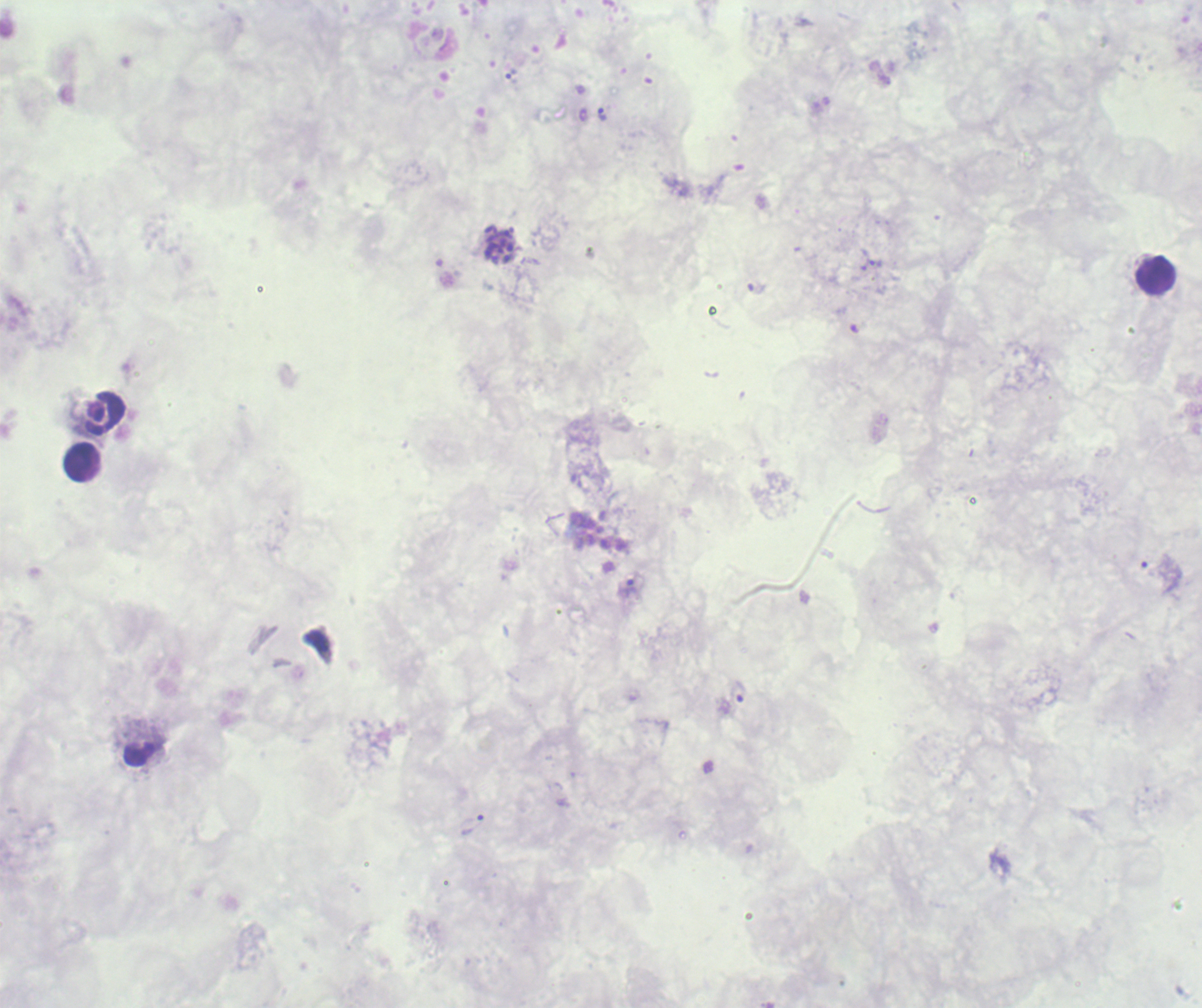
Approximate centers as {x, y} in pixels.
Summary:
  - Schizont locations: {499, 245}
  - Trophozoite locations: {602, 115}, {876, 263}, {629, 588}, {737, 692}, {473, 825}
  - Leukocyte locations: {1156, 275}, {106, 414}, {80, 461}, {139, 753}
  - Life-cycle stages observed: trophozoite, schizont
  - Magnification: 100x
  - Background quality: poor
  - Field of view: one from this slide
  - Image size: 1202×1008 pixels
  - Result: malaria parasites identified
  - Preparation: thick blood film
  - Context: previously used in a real diagnosis
  - Stain: Romanowsky